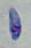
{
  "identification": "Toxoplasma gondii",
  "magnification": "1000x",
  "modality": "micrograph"
}